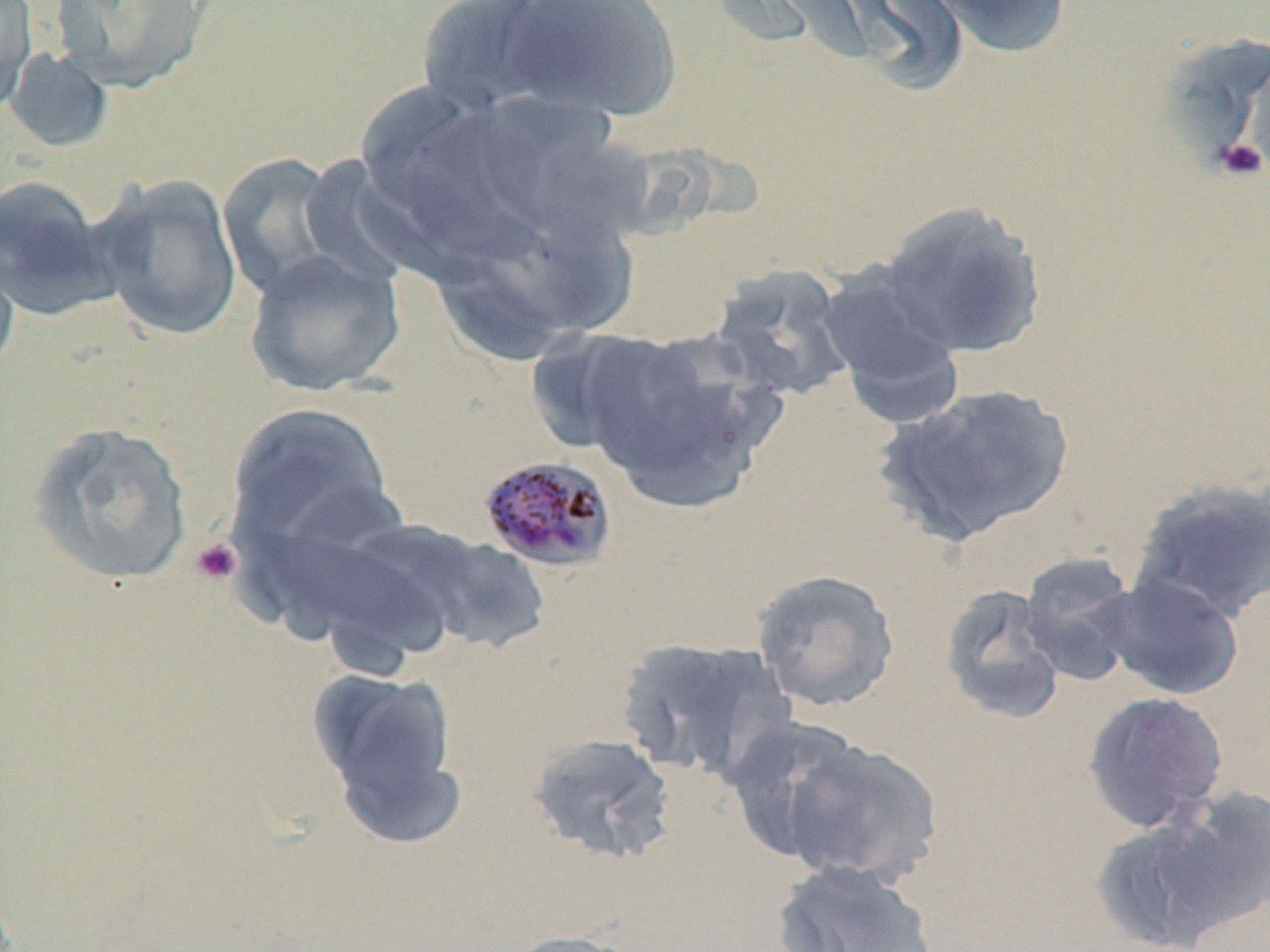

slide_level_diagnosis: Plasmodium malariae
uninfected_red_blood_cell_locations: 'approximate bounding boxes as (x1, y1, x2, y2) in pixels: (0, 0, 38, 117), (49, 0, 211, 95), (413, 0, 572, 115), (499, 0, 683, 121), (834, 0, 969, 96), (925, 0, 1072, 59), (1156, 33, 1270, 174), (1, 46, 116, 155), (345, 80, 472, 195), (409, 123, 547, 263), (541, 138, 664, 250), (217, 151, 357, 303), (92, 174, 244, 342), (0, 175, 118, 321), (876, 201, 1047, 359), (489, 212, 644, 330), (0, 241, 20, 380), (242, 248, 407, 398), (820, 262, 966, 423), (710, 264, 856, 402), (573, 329, 776, 512), (875, 382, 1074, 547), (224, 402, 398, 571), (24, 420, 195, 586), (1129, 479, 1270, 627), (393, 528, 554, 657), (252, 539, 449, 654), (1018, 553, 1142, 687), (751, 569, 900, 712), (1097, 573, 1245, 700), (938, 582, 1068, 724), (616, 635, 795, 787), (306, 666, 464, 838), (1081, 690, 1229, 834), (719, 712, 880, 868), (525, 732, 677, 866), (770, 735, 944, 888), (1158, 786, 1270, 937), (1090, 807, 1250, 952), (770, 859, 938, 952), (502, 930, 647, 952)'
platelet_locations: 'approximate bounding boxes as (x1, y1, x2, y2) in pixels: (1213, 137, 1268, 182), (189, 537, 243, 587)'
plasmodium_malariae_infected_red_blood_cell_locations: 'approximate bounding boxes as (x1, y1, x2, y2) in pixels: (477, 453, 619, 574)'
preparation: thin blood smear
field_of_view: single
modality: optical microscopy
stain: May-Grünwald-Giemsa
image_size: 1270×952 pixels
magnification: 1000x